Identify the preparation type.
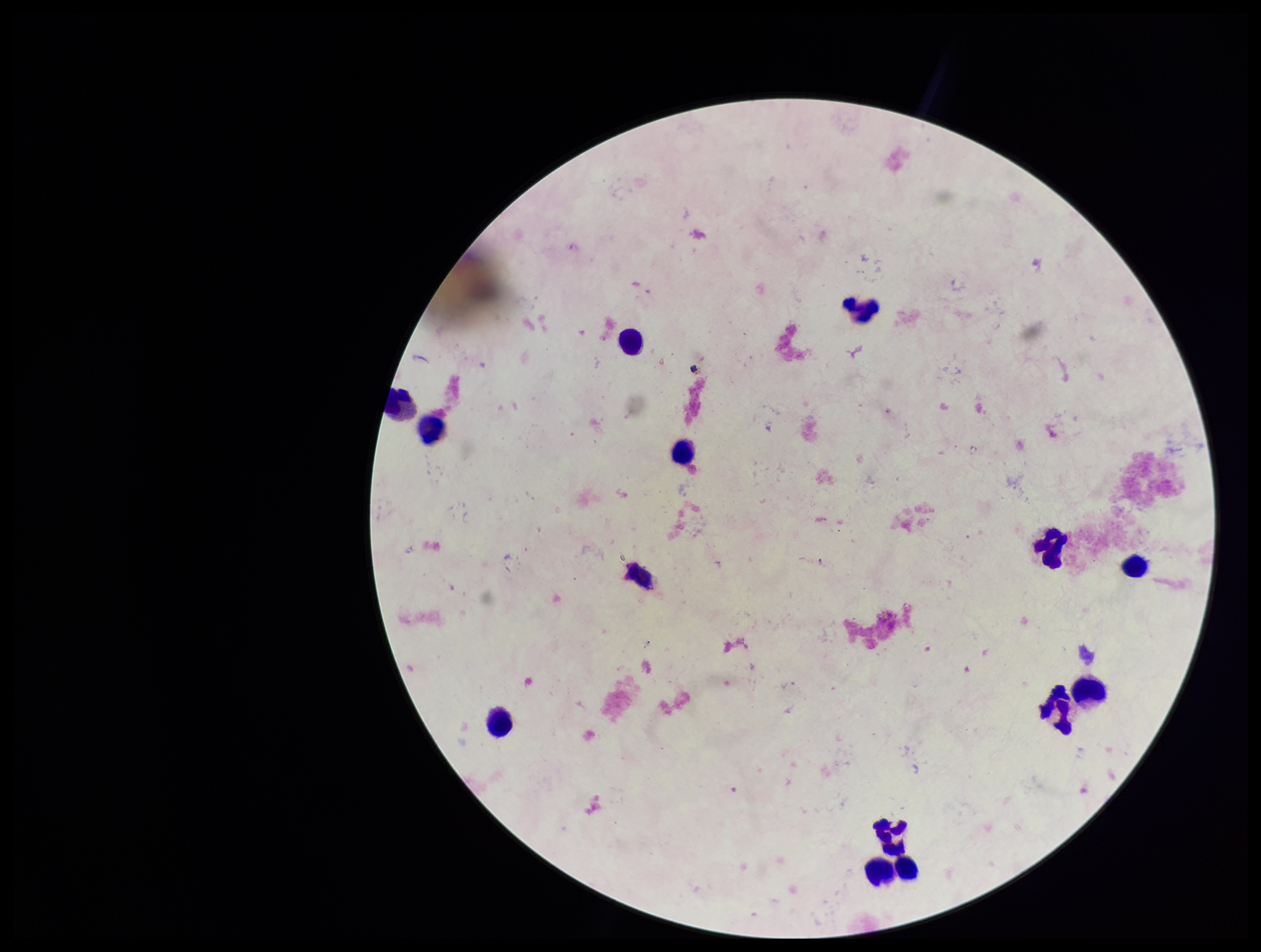

Thick.

Patient malaria status: negative. Plasmodium parasites: none seen. Parasite count: 0. Leukocyte count: 14. Single field of view. Giemsa stain. Image is 1261×952 pixels. Smartphone photograph taken through the eyepiece of a microscope.